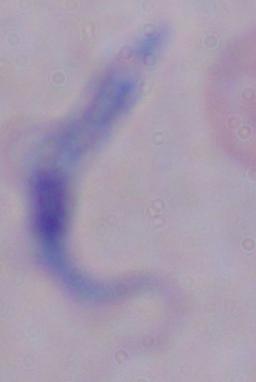
Summary:
  - Modality: photomicrograph
  - Magnification: 1000x
  - Identification: trypanosome